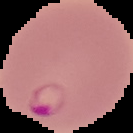 From a thin blood film. Malaria status: parasitized. Image is 133×133 pixels. The area outside the segmented cell region is set to black.